Identify the cell.
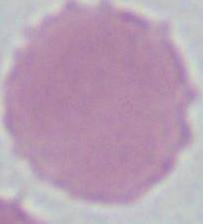

An erythrocyte.

Summary:
  - Magnification: 1000x
  - Modality: photomicrograph